Identify the parasite.
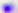
Toxoplasma gondii.

magnification = 400x
modality = photomicrograph